Locate and identify every blood parasite.
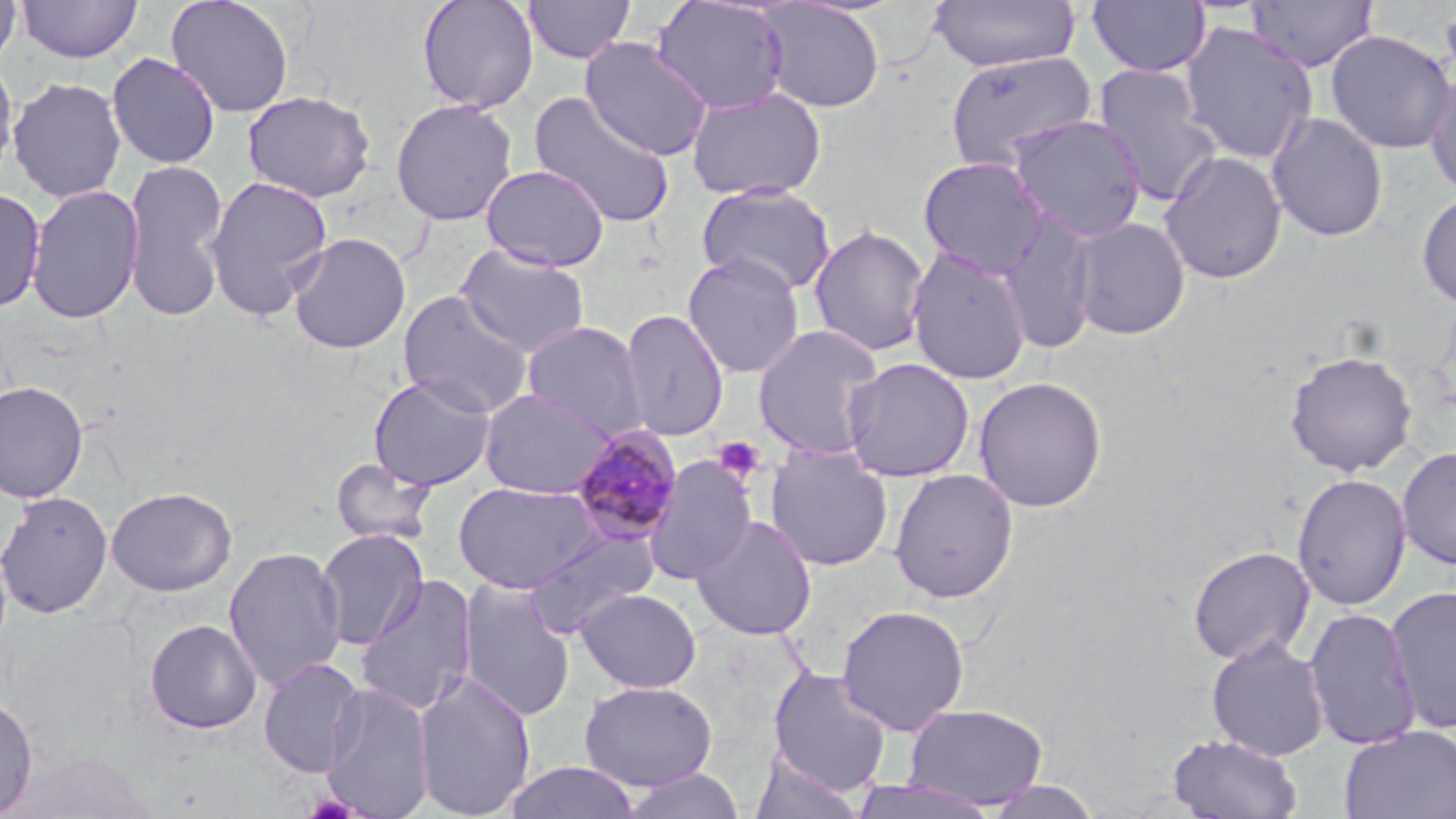
Approximate bounding boxes as [x1, y1, x2, y2] in pixels.
Plasmodium malariae-infected red blood cells: [570, 427, 684, 545].
No Plasmodium falciparum, Plasmodium ovale, Plasmodium vivax, Babesia divergens, or Trypanosoma brucei observed.

slide-level diagnosis = Plasmodium malariae
field of view = single
stain = May-Grünwald-Giemsa
platelet locations = approximate bounding boxes as [x1, y1, x2, y2] in pixels: [713, 437, 765, 482]
preparation = thin blood film
modality = light microscopy
uninfected red blood cell locations = approximate bounding boxes as [x1, y1, x2, y2] in pixels: [0, 0, 22, 72], [19, 0, 141, 63], [165, 0, 295, 118], [417, 0, 539, 113], [523, 0, 636, 64], [650, 0, 790, 115], [927, 0, 1082, 73], [1245, 0, 1378, 72], [757, 1, 886, 114], [1086, 1, 1211, 78], [1438, 1, 1456, 96], [1178, 20, 1319, 166], [1324, 29, 1455, 154], [580, 37, 713, 160], [944, 50, 1099, 173], [106, 52, 220, 169], [0, 55, 19, 184], [1092, 63, 1223, 206], [1424, 65, 1456, 201], [7, 76, 126, 203], [686, 86, 827, 201], [242, 90, 376, 202], [529, 91, 676, 229], [390, 97, 518, 226], [1265, 111, 1388, 242], [1005, 114, 1147, 243], [1158, 150, 1288, 285], [917, 156, 1052, 279], [121, 159, 230, 322], [481, 163, 610, 272], [203, 175, 334, 321], [696, 183, 837, 297], [26, 184, 144, 324], [0, 187, 46, 312], [1416, 190, 1456, 309], [995, 211, 1099, 355], [1068, 216, 1191, 340], [808, 224, 930, 358], [287, 232, 411, 354], [456, 243, 590, 358], [906, 245, 1032, 385], [682, 254, 805, 379], [398, 290, 534, 418], [618, 309, 730, 441], [521, 321, 649, 440], [751, 323, 885, 461], [1284, 350, 1418, 476], [841, 358, 975, 483], [368, 373, 497, 491], [973, 375, 1108, 512], [0, 381, 88, 503], [478, 388, 614, 500], [765, 444, 894, 571], [1397, 445, 1456, 571], [643, 456, 758, 585], [331, 457, 437, 547], [888, 468, 1019, 604], [1291, 472, 1412, 611], [453, 480, 603, 593], [105, 486, 236, 596], [0, 490, 114, 619], [690, 514, 818, 640], [521, 526, 661, 637], [314, 528, 429, 650], [1187, 544, 1315, 666], [223, 546, 347, 692], [355, 575, 478, 715], [457, 578, 576, 721], [1384, 585, 1456, 735], [575, 587, 701, 693], [836, 604, 971, 735], [1302, 607, 1421, 751], [143, 618, 263, 734], [1206, 637, 1330, 761], [258, 657, 367, 778], [767, 666, 894, 794], [413, 670, 537, 819], [579, 680, 718, 791], [320, 681, 435, 819], [0, 695, 38, 817], [902, 702, 1049, 809], [1339, 725, 1456, 819], [1167, 732, 1303, 818], [748, 753, 867, 819], [502, 761, 643, 818], [618, 768, 748, 819], [846, 778, 1004, 818], [980, 778, 1103, 819]
magnification = 1000x
image size = 1456×819 pixels